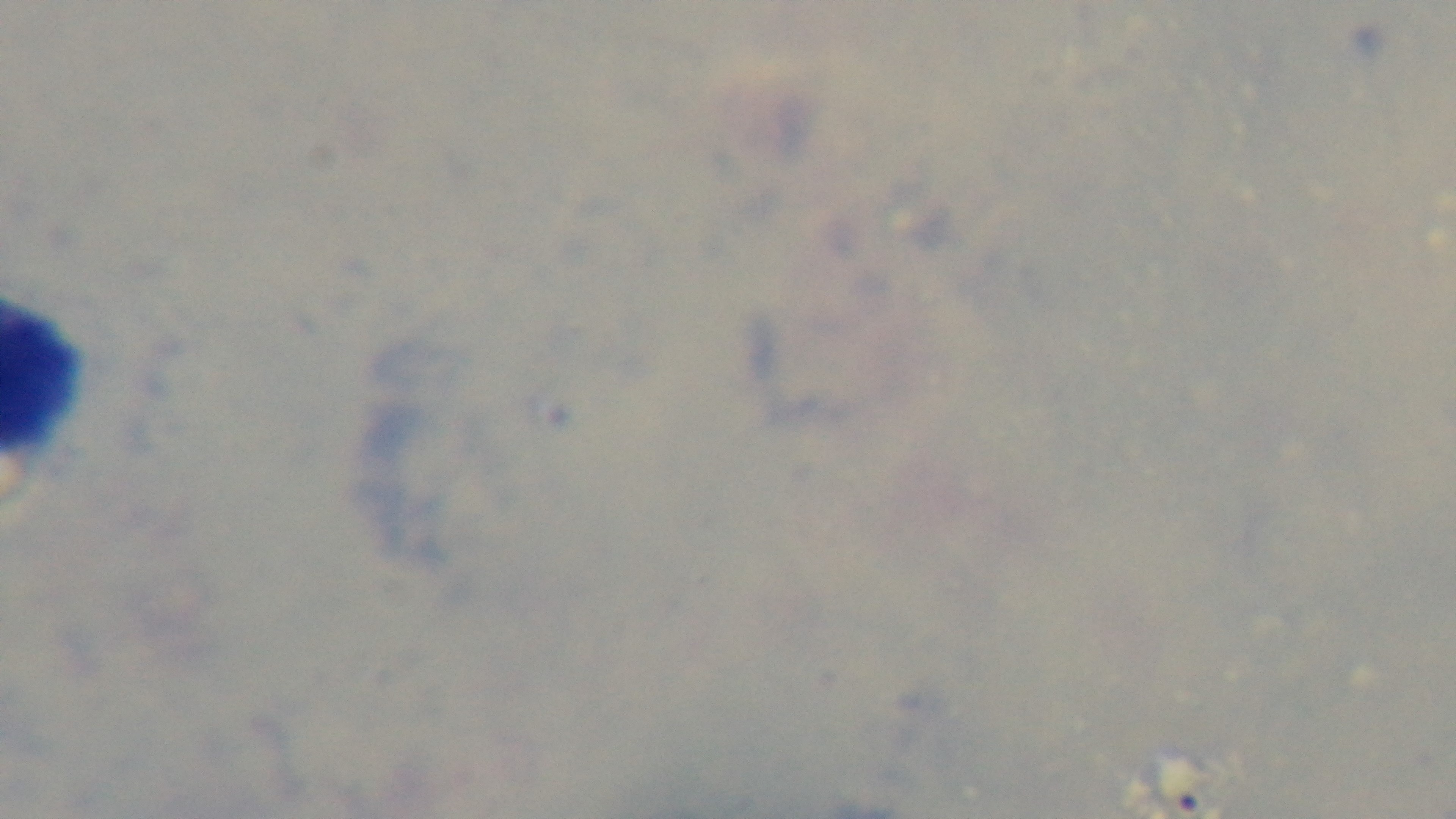
field of view = one from the slide
modality = light microscopy
stain = Giemsa
objective = 100x oil immersion
capture = mounted 4K digital camera
malaria status = uninfected
preparation = thick blood film